Classify this cell by malaria status.
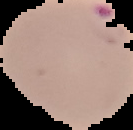
It is parasitized.

Summary:
  - Image size: 133×130 pixels
  - Image type: cell region segmented out of the field of view; surrounding area masked to black
  - Preparation: thin blood smear